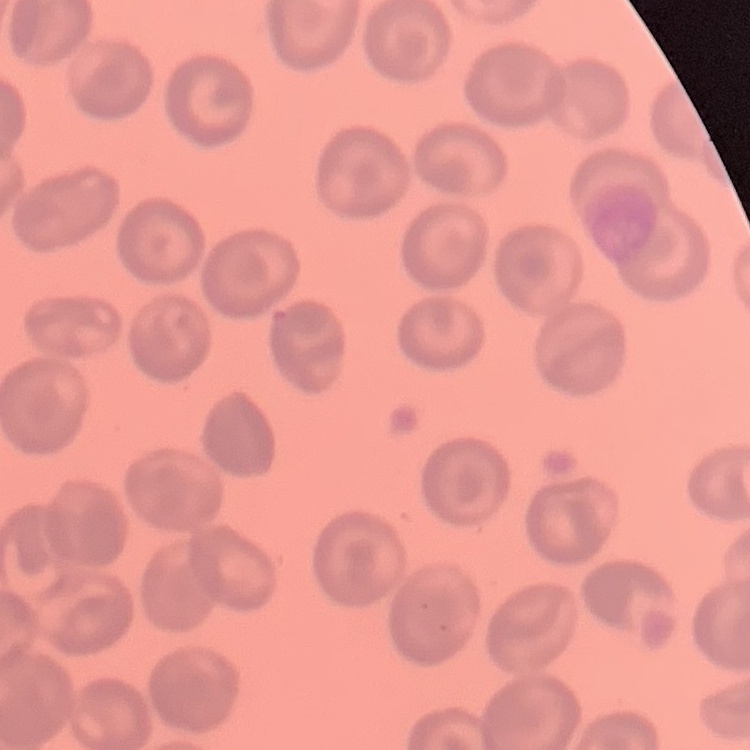

The red blood cells show no rouleaux formation. Square crop of a larger photomicrograph. Thin peripheral smear. Field's or Giemsa stain.